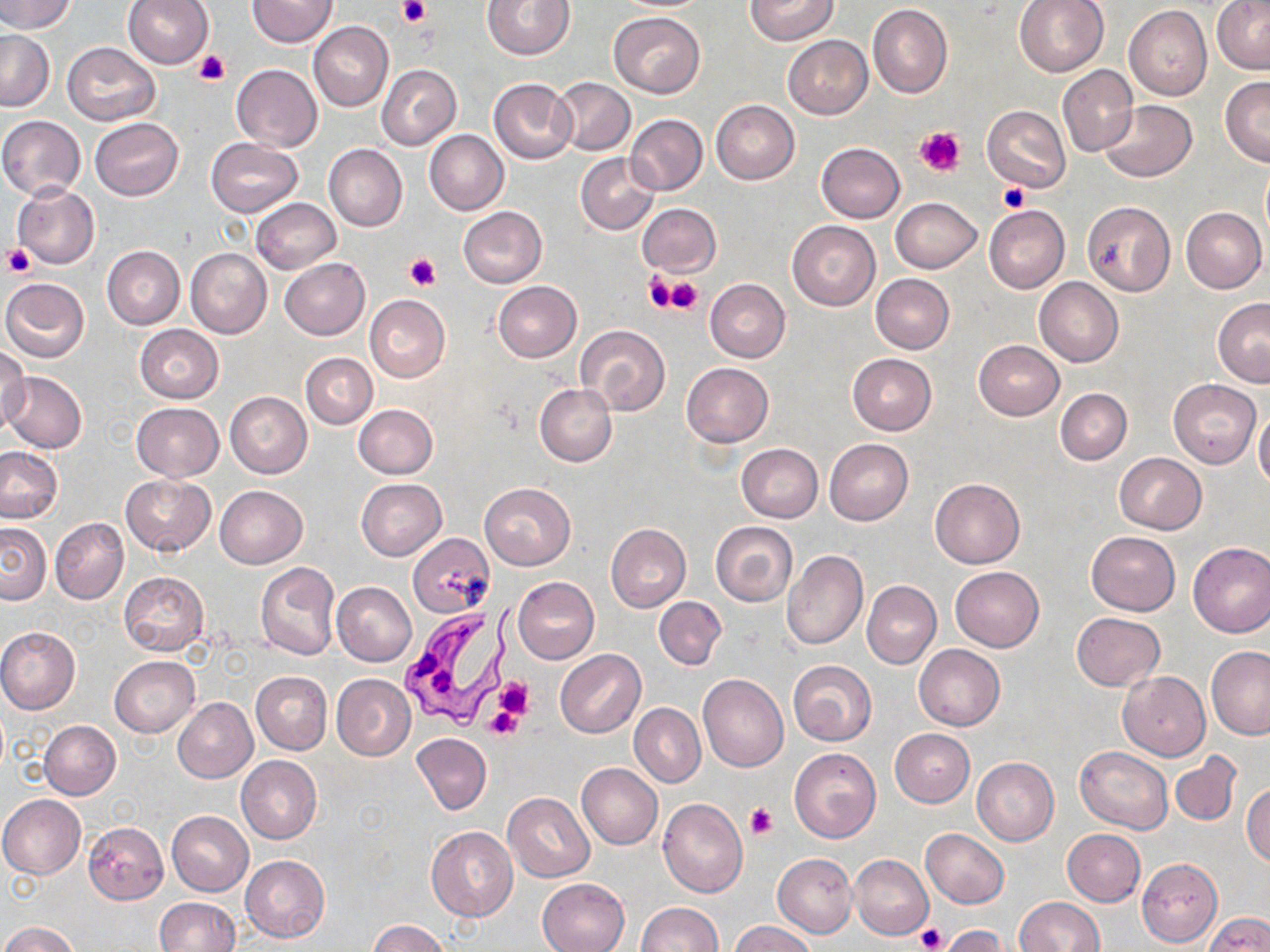
Approximate bounding boxes as (x1,y1)-(x2,y2) corner pairs in pixels. Trypanosoma brucei locations: (397,614)-(506,729). Platelet locations: (398,0)-(430,25), (193,48)-(230,87), (915,126)-(967,177), (997,183)-(1029,213), (3,245)-(37,278), (405,253)-(441,291), (645,270)-(690,313), (663,276)-(703,314), (493,677)-(534,722), (486,710)-(521,739), (745,804)-(777,839), (916,925)-(947,951). Uninfected red blood cell locations: (0,0)-(76,33), (122,0)-(213,67), (247,0)-(338,48), (481,0)-(574,59), (744,0)-(838,45), (1013,0)-(1109,77), (1212,2)-(1270,73), (867,4)-(952,100), (1124,6)-(1212,100), (609,11)-(705,97), (310,21)-(392,112), (0,30)-(53,112), (784,35)-(872,118), (62,42)-(160,125), (231,64)-(322,151), (377,64)-(461,151), (1058,65)-(1138,157), (552,77)-(635,155), (1220,77)-(1270,166), (488,78)-(577,164), (710,100)-(799,185), (1101,100)-(1196,182), (982,105)-(1071,191), (626,114)-(707,196), (0,116)-(86,199), (90,118)-(184,200), (424,130)-(508,215), (206,139)-(302,216), (816,142)-(905,223), (325,144)-(407,232), (576,154)-(660,235), (12,184)-(99,269), (891,197)-(982,273), (251,198)-(340,274), (1082,202)-(1176,296), (637,203)-(720,277), (984,205)-(1069,294), (458,207)-(547,287), (1181,207)-(1267,294), (787,221)-(881,311), (102,246)-(184,328), (185,247)-(272,339), (279,258)-(369,340), (870,273)-(954,354), (1035,277)-(1123,367), (1,278)-(90,362), (706,279)-(790,363), (493,281)-(581,362), (365,295)-(449,381), (1215,298)-(1270,387), (576,324)-(670,415), (135,325)-(223,403), (974,339)-(1064,419), (0,345)-(30,437), (301,353)-(377,430), (848,353)-(936,434), (681,363)-(773,447), (3,371)-(88,453), (1169,378)-(1261,468), (535,383)-(616,466), (1055,387)-(1131,465), (225,392)-(312,478), (132,402)-(224,481), (354,404)-(437,478), (1254,411)-(1270,491), (825,438)-(913,525), (738,443)-(823,522), (0,446)-(64,522), (1115,452)-(1206,533), (120,475)-(215,556), (929,477)-(1025,569), (357,478)-(447,560), (480,482)-(575,569), (216,486)-(307,567), (51,518)-(128,604), (0,522)-(51,605), (711,522)-(797,606), (606,523)-(691,612), (1086,531)-(1180,615), (407,534)-(494,618), (1187,542)-(1270,638), (782,550)-(868,650), (255,562)-(341,661), (950,566)-(1044,652), (119,572)-(209,656), (513,577)-(599,663), (862,581)-(940,668), (332,582)-(416,666), (654,597)-(727,670), (1072,612)-(1165,690), (0,627)-(80,714), (914,644)-(1004,730), (1206,647)-(1270,739), (555,650)-(645,738), (109,656)-(199,737), (788,660)-(876,745), (1117,671)-(1210,761), (251,672)-(332,755), (331,674)-(416,761), (698,675)-(788,771), (172,698)-(257,783), (630,704)-(704,787), (39,720)-(121,799), (889,728)-(974,807), (412,733)-(492,814), (1074,746)-(1172,833), (789,748)-(882,843), (1170,750)-(1243,826), (236,756)-(322,843), (972,758)-(1059,845), (577,763)-(663,849), (1243,782)-(1270,866), (504,793)-(595,882), (0,795)-(86,878), (658,798)-(748,896), (168,810)-(253,896), (84,822)-(168,904), (426,827)-(518,922), (920,829)-(1009,908), (1062,829)-(1146,906), (773,853)-(857,937), (850,854)-(934,940), (240,855)-(330,942), (1136,857)-(1222,947), (536,878)-(629,952), (155,897)-(239,951), (1014,897)-(1104,951), (634,903)-(721,952), (1203,912)-(1270,952), (370,920)-(449,952), (0,921)-(78,952), (730,921)-(817,952), (937,924)-(1003,951). Slide-level diagnosis: Trypanosoma brucei. May-Grünwald-Giemsa-stained preparation. Optical microscopy. Image is 1270×952 pixels. Single field of view. Thin blood smear. 1000x magnification.